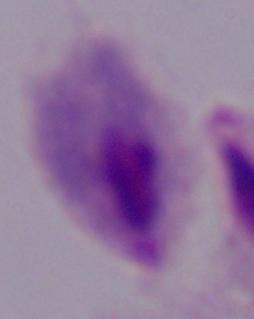

modality = photomicrograph
magnification = 1000x
identification = trichomonad